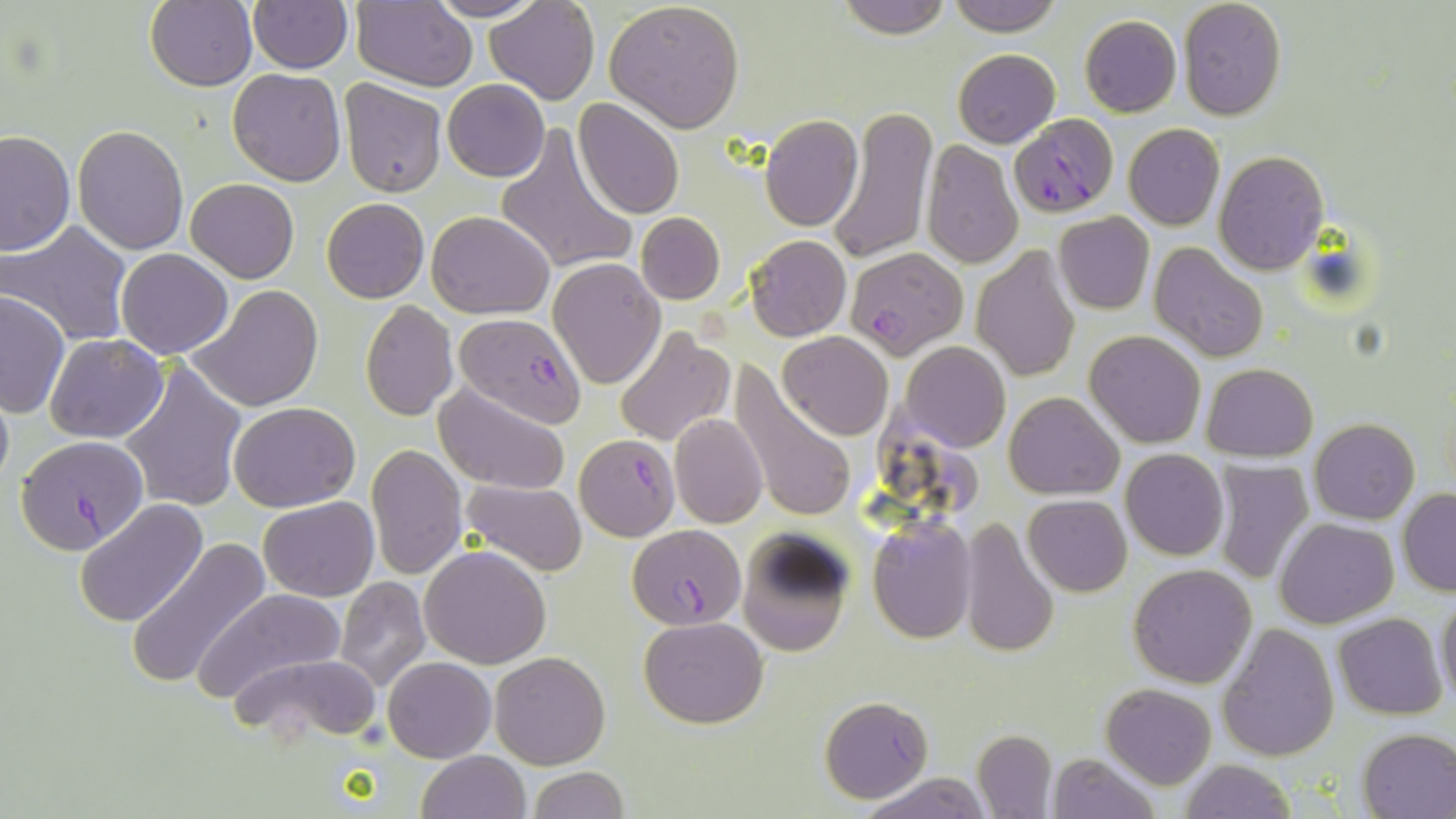 Approximate bounding boxes as named x1/y1/x2/y2 corners in pixels. Uninfected red blood cell locations: (x1=144, y1=0, x2=257, y2=90), (x1=426, y1=0, x2=547, y2=22), (x1=484, y1=0, x2=599, y2=105), (x1=837, y1=0, x2=952, y2=40), (x1=947, y1=0, x2=1063, y2=36), (x1=350, y1=1, x2=477, y2=89), (x1=604, y1=1, x2=746, y2=132), (x1=1179, y1=1, x2=1287, y2=119), (x1=249, y1=2, x2=351, y2=73), (x1=1079, y1=14, x2=1182, y2=117), (x1=953, y1=49, x2=1060, y2=147), (x1=228, y1=68, x2=345, y2=186), (x1=339, y1=78, x2=448, y2=199), (x1=443, y1=79, x2=549, y2=183), (x1=574, y1=99, x2=684, y2=220), (x1=828, y1=104, x2=938, y2=266), (x1=758, y1=114, x2=863, y2=231), (x1=1122, y1=124, x2=1224, y2=230), (x1=72, y1=125, x2=187, y2=255), (x1=496, y1=125, x2=638, y2=277), (x1=0, y1=128, x2=74, y2=256), (x1=921, y1=141, x2=1023, y2=269), (x1=1213, y1=151, x2=1328, y2=274), (x1=187, y1=178, x2=299, y2=282), (x1=321, y1=198, x2=429, y2=302), (x1=428, y1=210, x2=554, y2=318), (x1=636, y1=213, x2=724, y2=304), (x1=1053, y1=213, x2=1154, y2=314), (x1=3, y1=222, x2=135, y2=348), (x1=745, y1=234, x2=851, y2=341), (x1=1148, y1=242, x2=1268, y2=362), (x1=117, y1=249, x2=234, y2=360), (x1=973, y1=249, x2=1080, y2=381), (x1=548, y1=259, x2=665, y2=388), (x1=188, y1=285, x2=325, y2=413), (x1=0, y1=293, x2=70, y2=417), (x1=360, y1=300, x2=459, y2=420), (x1=615, y1=328, x2=732, y2=447), (x1=1085, y1=330, x2=1206, y2=449), (x1=777, y1=332, x2=893, y2=441), (x1=43, y1=333, x2=168, y2=443), (x1=901, y1=341, x2=1010, y2=451), (x1=120, y1=361, x2=248, y2=513), (x1=1202, y1=363, x2=1318, y2=460), (x1=728, y1=364, x2=859, y2=526), (x1=0, y1=379, x2=13, y2=495), (x1=432, y1=380, x2=571, y2=495), (x1=1004, y1=391, x2=1123, y2=498), (x1=229, y1=401, x2=360, y2=512), (x1=669, y1=414, x2=768, y2=528), (x1=1309, y1=419, x2=1420, y2=523), (x1=366, y1=443, x2=467, y2=582), (x1=1120, y1=450, x2=1228, y2=561), (x1=1211, y1=459, x2=1314, y2=583), (x1=459, y1=480, x2=586, y2=576), (x1=1398, y1=488, x2=1456, y2=595), (x1=1024, y1=495, x2=1132, y2=597), (x1=259, y1=497, x2=379, y2=602), (x1=74, y1=499, x2=207, y2=628), (x1=958, y1=516, x2=1058, y2=661), (x1=867, y1=517, x2=977, y2=643), (x1=1275, y1=518, x2=1399, y2=628), (x1=736, y1=531, x2=854, y2=658), (x1=126, y1=539, x2=270, y2=690), (x1=419, y1=546, x2=551, y2=667), (x1=1128, y1=563, x2=1257, y2=688), (x1=332, y1=576, x2=431, y2=693), (x1=192, y1=587, x2=345, y2=704), (x1=1435, y1=594, x2=1456, y2=708), (x1=1333, y1=612, x2=1448, y2=720), (x1=639, y1=616, x2=767, y2=728), (x1=1218, y1=622, x2=1339, y2=762), (x1=489, y1=652, x2=610, y2=770), (x1=231, y1=653, x2=384, y2=744), (x1=383, y1=657, x2=496, y2=763), (x1=1102, y1=682, x2=1215, y2=788), (x1=820, y1=696, x2=933, y2=803), (x1=1357, y1=728, x2=1456, y2=817), (x1=971, y1=730, x2=1056, y2=817), (x1=416, y1=751, x2=532, y2=819), (x1=1047, y1=753, x2=1160, y2=818), (x1=1178, y1=760, x2=1297, y2=818), (x1=529, y1=766, x2=628, y2=819), (x1=858, y1=773, x2=992, y2=818). Plasmodium falciparum-infected red blood cell locations: (x1=1009, y1=114, x2=1119, y2=217), (x1=844, y1=248, x2=968, y2=360), (x1=453, y1=313, x2=587, y2=427), (x1=18, y1=434, x2=150, y2=559), (x1=574, y1=435, x2=679, y2=540), (x1=629, y1=524, x2=745, y2=628). Slide-level diagnosis: Plasmodium falciparum. Image is 1456×819 pixels. May-Grünwald-Giemsa-stained preparation. Single field of view. 1000x magnification. Thin blood smear. Optical microscopy.